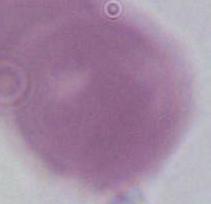 A red blood cell is shown. Photomicrograph. Captured at 1000x magnification.